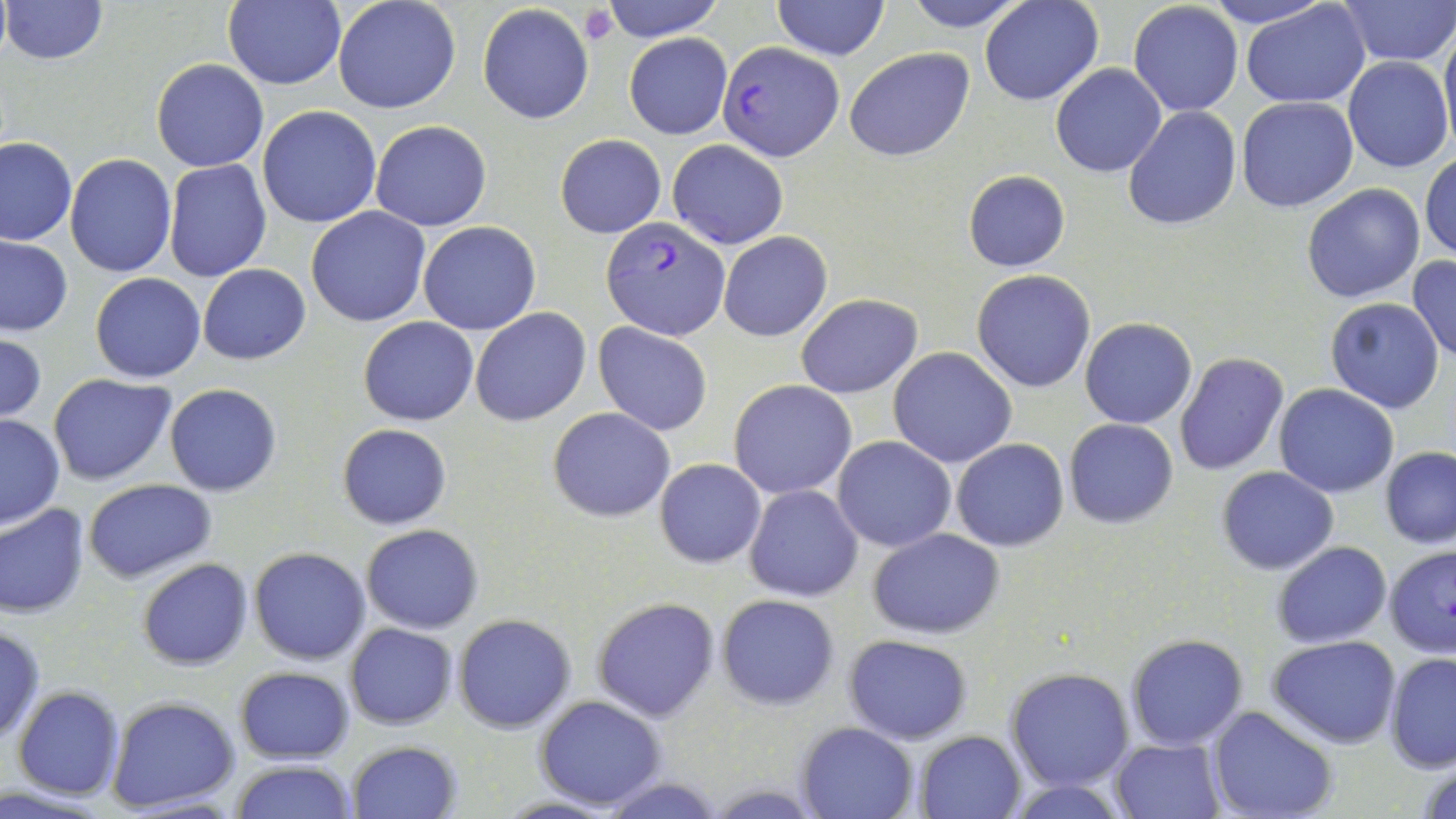

slide-level diagnosis = Plasmodium falciparum
uninfected red blood cell locations = approximate bounding boxes as [x1, y1, x2, y2] in pixels: [1, 0, 108, 65], [223, 0, 345, 89], [332, 0, 462, 115], [599, 0, 727, 42], [771, 0, 890, 62], [902, 0, 1030, 31], [981, 0, 1104, 105], [1195, 0, 1334, 26], [1337, 0, 1453, 64], [1240, 1, 1370, 108], [1128, 2, 1243, 117], [477, 4, 595, 125], [1439, 20, 1456, 148], [623, 33, 732, 138], [844, 47, 974, 161], [1343, 57, 1452, 172], [152, 58, 268, 172], [1051, 63, 1166, 177], [1236, 95, 1359, 212], [257, 105, 383, 229], [1124, 105, 1241, 232], [370, 120, 492, 231], [554, 135, 665, 239], [0, 136, 77, 246], [668, 139, 789, 250], [1420, 152, 1455, 262], [64, 154, 177, 276], [163, 158, 271, 282], [962, 170, 1071, 272], [1302, 183, 1425, 304], [306, 207, 432, 327], [418, 222, 542, 334], [718, 232, 832, 340], [0, 236, 73, 336], [1406, 254, 1456, 363], [197, 264, 311, 364], [971, 270, 1096, 393], [90, 273, 206, 384], [795, 293, 922, 398], [1325, 297, 1445, 414], [471, 309, 591, 426], [357, 316, 479, 426], [1080, 318, 1197, 428], [593, 323, 712, 435], [0, 333, 47, 424], [888, 347, 1018, 467], [1174, 353, 1289, 476], [48, 374, 177, 486], [728, 378, 857, 499], [164, 384, 282, 497], [1275, 385, 1398, 497], [548, 407, 676, 522], [0, 414, 65, 529], [1063, 418, 1178, 528], [336, 423, 453, 530], [832, 437, 956, 552], [952, 438, 1069, 551], [1380, 446, 1456, 548], [654, 458, 766, 568], [1216, 465, 1339, 575], [82, 478, 219, 585], [745, 484, 863, 602], [0, 502, 90, 618], [361, 524, 484, 634], [867, 529, 1004, 638], [1271, 540, 1392, 648], [1384, 546, 1455, 658], [248, 547, 372, 665], [136, 559, 252, 670], [716, 594, 840, 710], [591, 597, 720, 721], [453, 613, 576, 733], [345, 622, 457, 730], [0, 627, 45, 744], [1124, 634, 1249, 751], [844, 635, 973, 745], [1266, 636, 1401, 748], [1385, 653, 1455, 774], [233, 665, 355, 764], [1006, 667, 1134, 790], [12, 686, 125, 801], [534, 694, 667, 809], [107, 696, 240, 810], [1207, 707, 1338, 819], [798, 720, 918, 819], [916, 730, 1024, 817], [1110, 736, 1225, 819], [346, 740, 463, 819], [1416, 753, 1456, 819], [229, 761, 359, 819], [599, 777, 732, 818], [1007, 778, 1131, 817], [0, 784, 115, 818]
platelet locations = approximate bounding boxes as [x1, y1, x2, y2] in pixels: [577, 5, 617, 45]
modality = optical microscopy
Plasmodium falciparum-infected red blood cell locations = approximate bounding boxes as [x1, y1, x2, y2] in pixels: [720, 42, 843, 161], [601, 217, 730, 340]
field of view = single
magnification = 1000x
image size = 1456×819 pixels
preparation = thin blood smear
stain = May-Grünwald-Giemsa